Locate and identify every blood parasite.
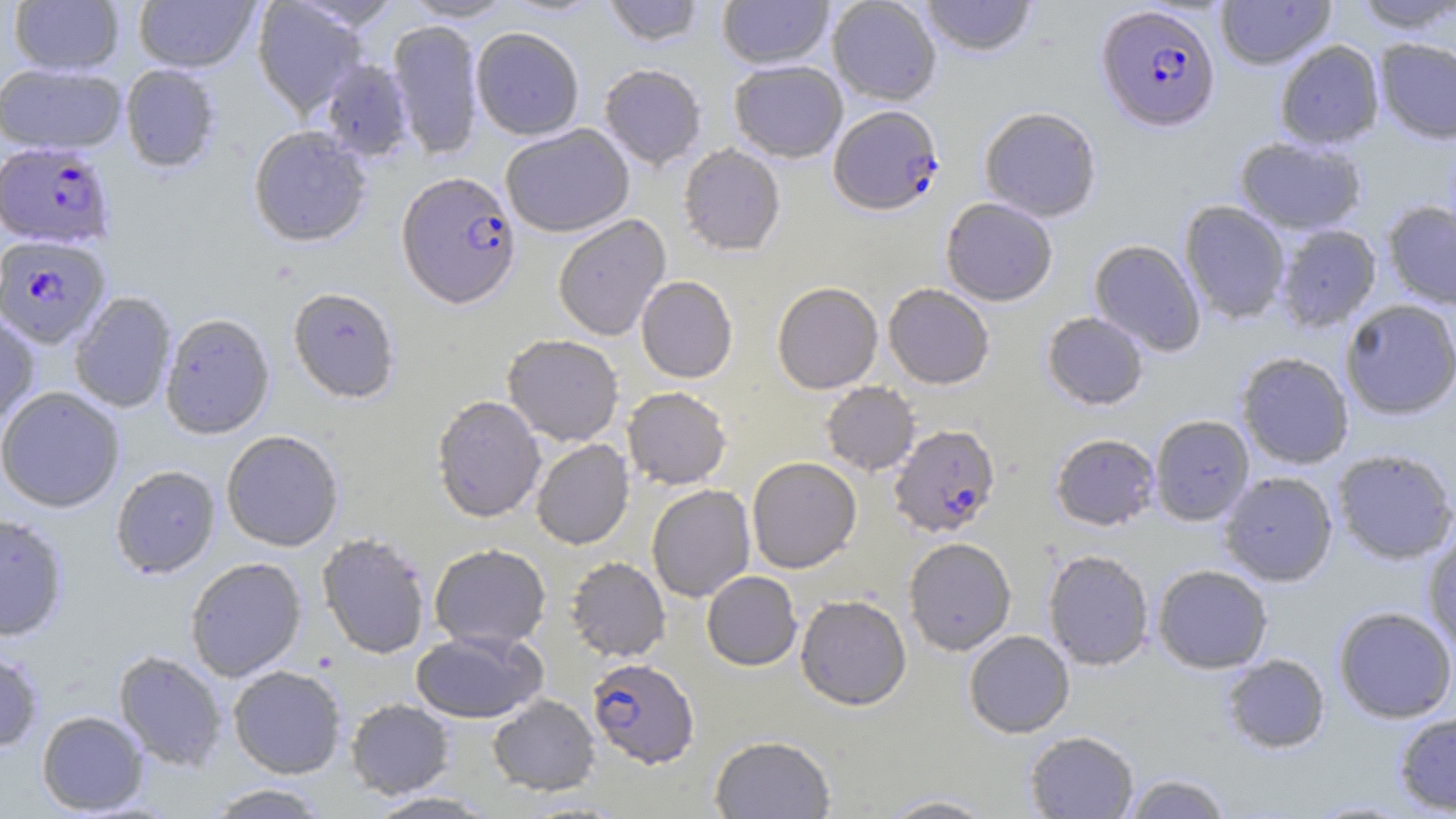
Approximate bounding boxes as named x1/y1/x2/y2 corners in pixels.
Plasmodium falciparum-infected red blood cells: (x1=1097, y1=4, x2=1220, y2=132), (x1=828, y1=105, x2=944, y2=215), (x1=0, y1=142, x2=114, y2=250), (x1=397, y1=171, x2=522, y2=309), (x1=0, y1=235, x2=111, y2=348), (x1=889, y1=423, x2=1001, y2=538), (x1=587, y1=658, x2=699, y2=768).
No Plasmodium ovale, Plasmodium malariae, Plasmodium vivax, Babesia divergens, or Trypanosoma brucei observed.

{
  "slide_level_diagnosis": "Plasmodium falciparum",
  "stain": "May-Grünwald-Giemsa",
  "image_size": "1456×819 pixels",
  "uninfected_red_blood_cell_locations": "approximate bounding boxes as named x1/y1/x2/y2 corners in pixels: (x1=134, y1=0, x2=259, y2=73), (x1=252, y1=0, x2=368, y2=117), (x1=402, y1=0, x2=517, y2=22), (x1=601, y1=0, x2=707, y2=47), (x1=718, y1=0, x2=834, y2=68), (x1=827, y1=0, x2=942, y2=105), (x1=919, y1=0, x2=1038, y2=57), (x1=1215, y1=0, x2=1336, y2=70), (x1=1349, y1=0, x2=1456, y2=33), (x1=9, y1=1, x2=124, y2=76), (x1=387, y1=19, x2=483, y2=159), (x1=471, y1=27, x2=584, y2=140), (x1=1374, y1=37, x2=1456, y2=144), (x1=1274, y1=40, x2=1385, y2=150), (x1=318, y1=59, x2=414, y2=162), (x1=728, y1=60, x2=848, y2=162), (x1=0, y1=63, x2=126, y2=155), (x1=599, y1=63, x2=707, y2=170), (x1=120, y1=64, x2=222, y2=173), (x1=979, y1=106, x2=1102, y2=222), (x1=501, y1=124, x2=634, y2=237), (x1=248, y1=126, x2=372, y2=247), (x1=1234, y1=136, x2=1367, y2=235), (x1=679, y1=144, x2=786, y2=256), (x1=940, y1=197, x2=1058, y2=306), (x1=1179, y1=201, x2=1291, y2=324), (x1=1382, y1=201, x2=1456, y2=309), (x1=553, y1=214, x2=671, y2=341), (x1=1275, y1=224, x2=1381, y2=332), (x1=1089, y1=239, x2=1206, y2=357), (x1=636, y1=276, x2=738, y2=383), (x1=772, y1=281, x2=883, y2=394), (x1=883, y1=283, x2=995, y2=390), (x1=288, y1=287, x2=401, y2=403), (x1=69, y1=292, x2=177, y2=413), (x1=1339, y1=300, x2=1456, y2=420), (x1=1042, y1=312, x2=1149, y2=410), (x1=0, y1=313, x2=40, y2=428), (x1=160, y1=313, x2=275, y2=439), (x1=503, y1=334, x2=624, y2=446), (x1=1236, y1=351, x2=1354, y2=469), (x1=820, y1=382, x2=920, y2=476), (x1=0, y1=386, x2=125, y2=513), (x1=623, y1=387, x2=732, y2=490), (x1=431, y1=394, x2=546, y2=523), (x1=1150, y1=415, x2=1255, y2=526), (x1=221, y1=430, x2=344, y2=552), (x1=1050, y1=432, x2=1160, y2=531), (x1=531, y1=439, x2=634, y2=549), (x1=1332, y1=448, x2=1456, y2=565), (x1=746, y1=456, x2=862, y2=573), (x1=111, y1=465, x2=221, y2=578), (x1=1218, y1=470, x2=1338, y2=587), (x1=646, y1=484, x2=756, y2=602), (x1=0, y1=514, x2=70, y2=641), (x1=1422, y1=529, x2=1456, y2=655), (x1=316, y1=532, x2=432, y2=659), (x1=903, y1=537, x2=1016, y2=656), (x1=429, y1=543, x2=552, y2=649), (x1=1042, y1=549, x2=1154, y2=670), (x1=565, y1=556, x2=671, y2=662), (x1=185, y1=557, x2=307, y2=681), (x1=1152, y1=564, x2=1272, y2=674), (x1=701, y1=571, x2=803, y2=671), (x1=795, y1=594, x2=911, y2=710), (x1=1333, y1=605, x2=1456, y2=723), (x1=964, y1=629, x2=1075, y2=737), (x1=410, y1=630, x2=547, y2=723), (x1=0, y1=645, x2=44, y2=753), (x1=113, y1=650, x2=227, y2=770), (x1=1221, y1=653, x2=1330, y2=754), (x1=228, y1=665, x2=347, y2=778), (x1=487, y1=694, x2=600, y2=796), (x1=345, y1=698, x2=455, y2=799), (x1=37, y1=710, x2=149, y2=815), (x1=1394, y1=710, x2=1456, y2=815), (x1=1024, y1=730, x2=1139, y2=818), (x1=709, y1=735, x2=836, y2=818), (x1=1121, y1=773, x2=1233, y2=818), (x1=203, y1=783, x2=333, y2=818), (x1=363, y1=791, x2=501, y2=818), (x1=876, y1=793, x2=1000, y2=818), (x1=1302, y1=798, x2=1420, y2=818)",
  "magnification": "1000x",
  "modality": "optical microscopy",
  "field_of_view": "single",
  "preparation": "thin blood smear"
}